Report the malaria status of this cell.
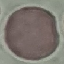
It is uninfected.

capture = smartphone camera at the microscope eyepiece
preparation = thin blood smear
stain = Giemsa
image type = cell patch, automatically extracted from a larger field of view and resized to 64 × 64 pixels